Assess the morphology of the erythrocytes.
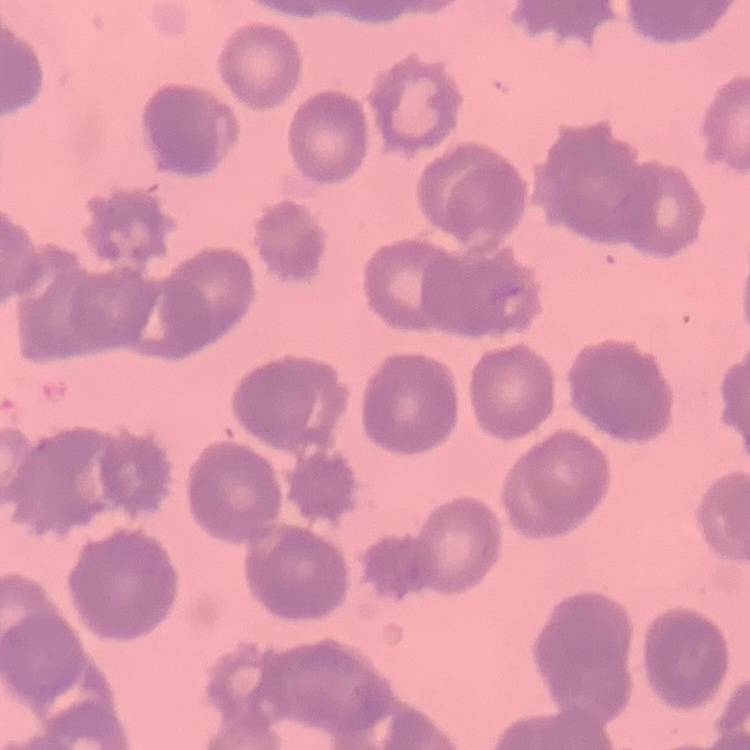
Rouleaux formation.

preparation = thin blood smear
image type = one tile cut from a larger photomicrograph
stain = Field's or Giemsa